Comment on the morphology of the red blood cells.
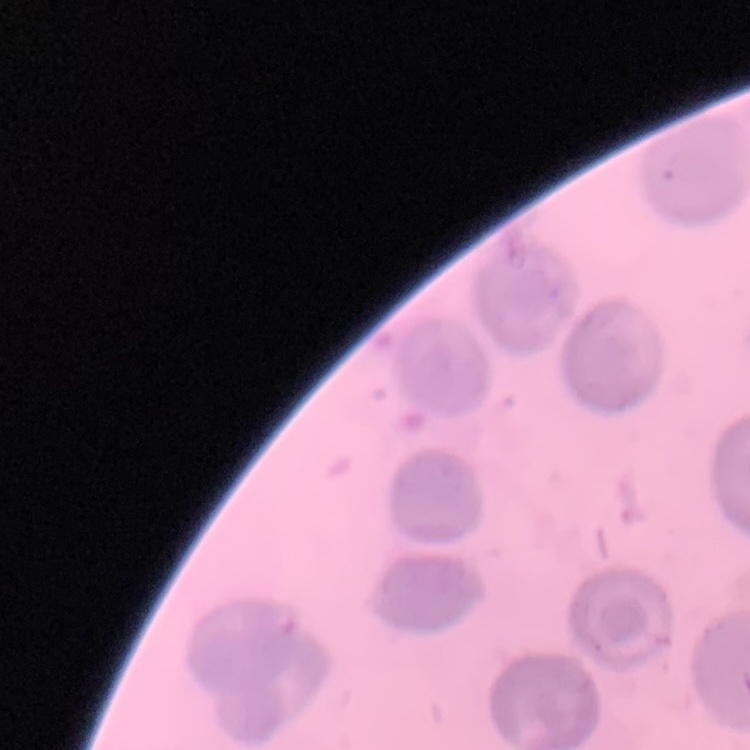
They show no rouleaux formation.

Thin peripheral smear. Stained with either Field's or Giemsa. Square crop of a larger photomicrograph.